Identify the blood parasite species.
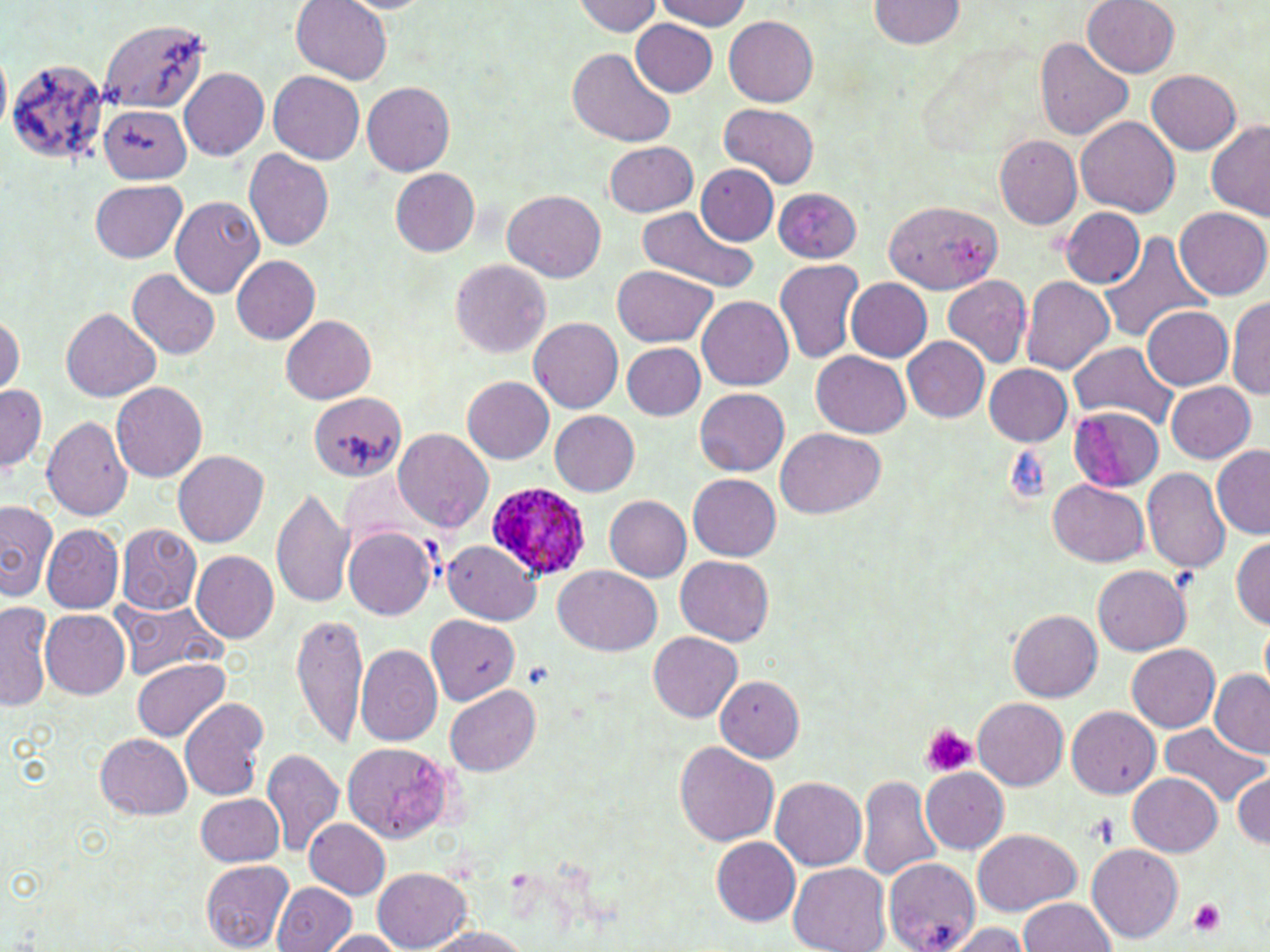

Plasmodium ovale.

Approximate bounding boxes as named x1/y1/x2/y2 corners in pixels. Uninfected red blood cell locations: (x1=656, y1=0, x2=752, y2=31), (x1=870, y1=0, x2=966, y2=48), (x1=572, y1=1, x2=661, y2=37), (x1=1083, y1=1, x2=1180, y2=77), (x1=293, y1=2, x2=392, y2=82), (x1=724, y1=15, x2=819, y2=105), (x1=631, y1=19, x2=717, y2=97), (x1=99, y1=20, x2=208, y2=113), (x1=1034, y1=37, x2=1133, y2=141), (x1=567, y1=47, x2=676, y2=148), (x1=0, y1=52, x2=11, y2=134), (x1=6, y1=57, x2=110, y2=167), (x1=180, y1=67, x2=269, y2=160), (x1=268, y1=70, x2=364, y2=164), (x1=1147, y1=70, x2=1241, y2=154), (x1=362, y1=82, x2=455, y2=176), (x1=720, y1=104, x2=820, y2=190), (x1=101, y1=105, x2=192, y2=183), (x1=1076, y1=115, x2=1181, y2=216), (x1=1206, y1=120, x2=1270, y2=219), (x1=994, y1=134, x2=1082, y2=228), (x1=604, y1=141, x2=698, y2=217), (x1=244, y1=149, x2=334, y2=250), (x1=695, y1=164, x2=779, y2=246), (x1=392, y1=169, x2=480, y2=255), (x1=89, y1=179, x2=186, y2=262), (x1=771, y1=187, x2=861, y2=263), (x1=503, y1=188, x2=605, y2=282), (x1=170, y1=196, x2=264, y2=298), (x1=884, y1=199, x2=1002, y2=295), (x1=636, y1=206, x2=757, y2=291), (x1=1061, y1=207, x2=1146, y2=288), (x1=1176, y1=207, x2=1269, y2=300), (x1=1097, y1=231, x2=1211, y2=345), (x1=229, y1=254, x2=319, y2=345), (x1=773, y1=257, x2=863, y2=364), (x1=450, y1=259, x2=549, y2=358), (x1=613, y1=265, x2=716, y2=347), (x1=128, y1=270, x2=220, y2=359), (x1=942, y1=274, x2=1032, y2=369), (x1=1021, y1=276, x2=1115, y2=374), (x1=845, y1=278, x2=933, y2=361), (x1=1228, y1=295, x2=1270, y2=400), (x1=697, y1=296, x2=794, y2=390), (x1=1142, y1=306, x2=1232, y2=389), (x1=61, y1=307, x2=161, y2=401), (x1=0, y1=313, x2=22, y2=397), (x1=281, y1=315, x2=375, y2=402), (x1=529, y1=316, x2=623, y2=413), (x1=903, y1=337, x2=989, y2=423), (x1=1068, y1=341, x2=1179, y2=426), (x1=621, y1=343, x2=706, y2=418), (x1=812, y1=349, x2=912, y2=436), (x1=983, y1=364, x2=1073, y2=446), (x1=463, y1=377, x2=555, y2=463), (x1=1, y1=379, x2=47, y2=478), (x1=1165, y1=381, x2=1256, y2=463), (x1=111, y1=382, x2=207, y2=483), (x1=695, y1=388, x2=789, y2=475), (x1=308, y1=390, x2=407, y2=481), (x1=1069, y1=408, x2=1166, y2=494), (x1=549, y1=410, x2=640, y2=496), (x1=41, y1=415, x2=133, y2=521), (x1=776, y1=427, x2=887, y2=517), (x1=393, y1=429, x2=494, y2=532), (x1=1211, y1=444, x2=1270, y2=536), (x1=173, y1=450, x2=270, y2=547), (x1=1141, y1=466, x2=1231, y2=572), (x1=688, y1=473, x2=781, y2=561), (x1=1049, y1=478, x2=1150, y2=565), (x1=271, y1=485, x2=354, y2=609), (x1=604, y1=495, x2=691, y2=580), (x1=1, y1=500, x2=55, y2=601), (x1=43, y1=523, x2=124, y2=612), (x1=116, y1=523, x2=201, y2=614), (x1=343, y1=525, x2=435, y2=620), (x1=1232, y1=535, x2=1270, y2=629), (x1=442, y1=539, x2=540, y2=623), (x1=191, y1=550, x2=279, y2=643), (x1=676, y1=555, x2=774, y2=645), (x1=1093, y1=565, x2=1192, y2=656), (x1=554, y1=566, x2=662, y2=657), (x1=114, y1=599, x2=226, y2=678), (x1=0, y1=602, x2=53, y2=712), (x1=40, y1=609, x2=130, y2=699), (x1=1008, y1=609, x2=1102, y2=701), (x1=291, y1=612, x2=369, y2=747), (x1=426, y1=614, x2=519, y2=704), (x1=1260, y1=620, x2=1270, y2=694), (x1=649, y1=632, x2=742, y2=721), (x1=1127, y1=643, x2=1218, y2=734), (x1=355, y1=644, x2=445, y2=746), (x1=132, y1=660, x2=231, y2=742), (x1=1210, y1=669, x2=1270, y2=756), (x1=714, y1=674, x2=806, y2=762), (x1=446, y1=686, x2=540, y2=776), (x1=972, y1=697, x2=1069, y2=789), (x1=179, y1=698, x2=271, y2=801), (x1=1066, y1=706, x2=1161, y2=799), (x1=1159, y1=724, x2=1266, y2=808), (x1=95, y1=733, x2=193, y2=820), (x1=676, y1=741, x2=779, y2=846), (x1=340, y1=742, x2=459, y2=841), (x1=262, y1=748, x2=342, y2=855), (x1=921, y1=768, x2=1008, y2=853), (x1=1232, y1=772, x2=1269, y2=850), (x1=1130, y1=773, x2=1221, y2=857), (x1=858, y1=775, x2=941, y2=881), (x1=770, y1=776, x2=867, y2=871), (x1=195, y1=793, x2=285, y2=866), (x1=306, y1=819, x2=391, y2=898), (x1=972, y1=827, x2=1082, y2=914), (x1=712, y1=837, x2=799, y2=925), (x1=1088, y1=843, x2=1184, y2=942), (x1=883, y1=856, x2=982, y2=951), (x1=201, y1=859, x2=293, y2=952), (x1=789, y1=863, x2=891, y2=952), (x1=374, y1=868, x2=471, y2=951), (x1=273, y1=882, x2=355, y2=951), (x1=1018, y1=897, x2=1118, y2=951), (x1=943, y1=923, x2=1034, y2=952), (x1=419, y1=928, x2=535, y2=952), (x1=319, y1=930, x2=408, y2=951). Plasmodium ovale-infected red blood cell locations: (x1=483, y1=480, x2=592, y2=584). Platelet locations: (x1=920, y1=723, x2=975, y2=778), (x1=1086, y1=813, x2=1123, y2=849), (x1=1187, y1=899, x2=1227, y2=936). 1000x magnification. Single field of view. Light microscopy. Thin blood film. Image is 1270×952 pixels. May-Grünwald-Giemsa stain.